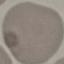

Summary:
  - Malaria status: uninfected
  - Capture: smartphone camera at the microscope eyepiece
  - Preparation: thin smear
  - Stain: Giemsa
  - Image type: automatically extracted cell patch, resized to 64 × 64 pixels